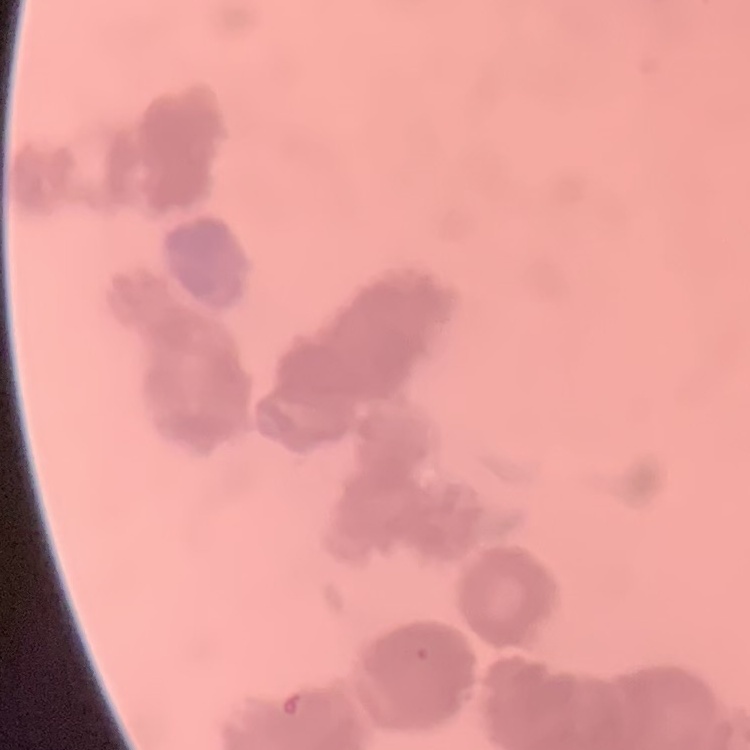

erythrocyte morphology = rouleaux formation
stain = Field's or Giemsa
image type = square crop of a larger photomicrograph
preparation = thin blood film